Locate every malaria parasite.
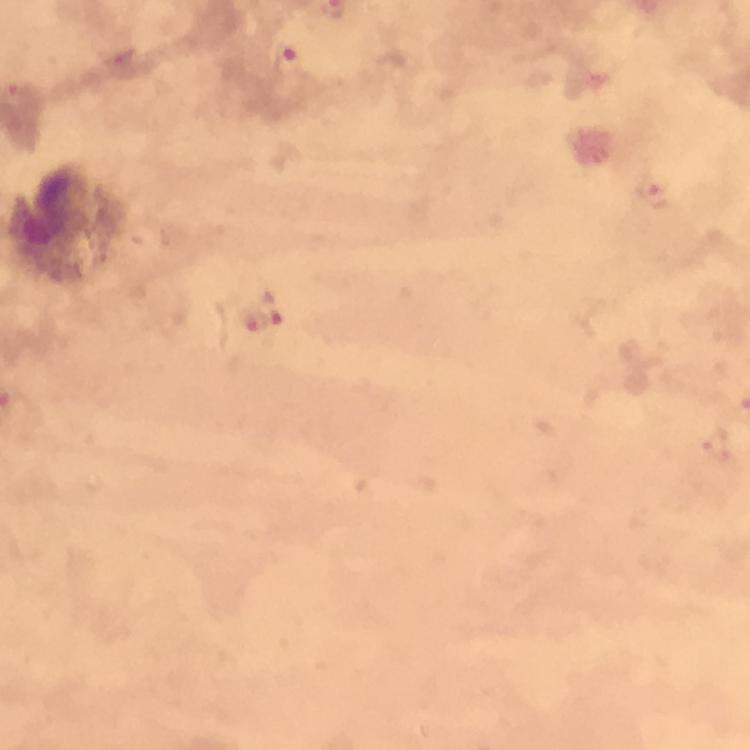

Approximate centers as {x, y} in pixels.
Malaria parasites: {122, 61}, {288, 62}, {20, 96}, {654, 191}, {275, 309}, {249, 324}, {717, 447}.

preparation = thick blood smear
cropped from = one field of view
leukocyte locations = approximate centers as {x, y} in pixels: {65, 224}
immersion oil = used
capture = smartphone mounted on the microscope
context = from a malaria diagnostic workup
magnification = 100x
stain = Giemsa
image size = 750×750 pixels